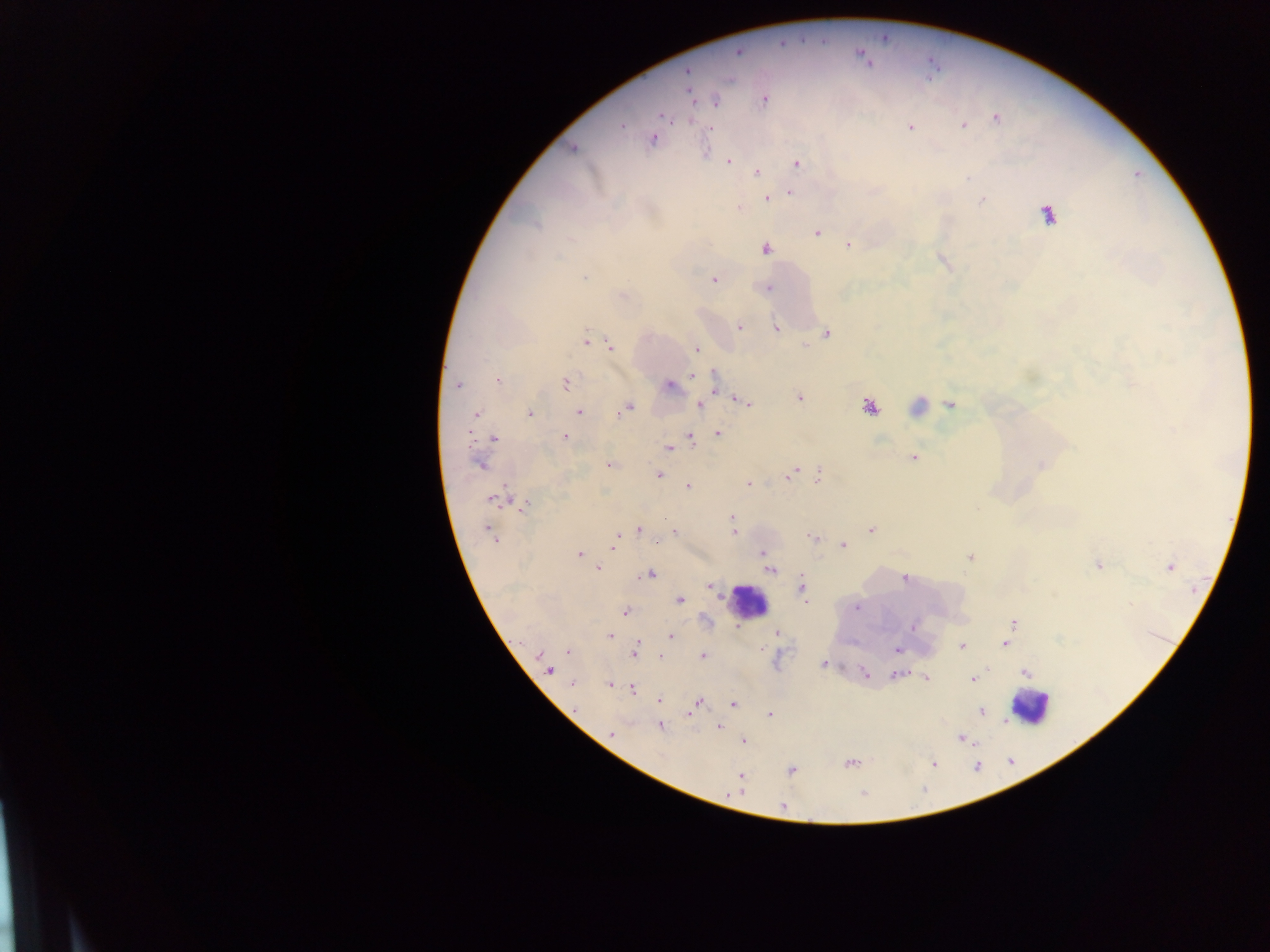

Approximate centers as x y in pixels.
Summary:
  - Leukocyte locations: 747 601; 1030 707
  - Plasmodium parasite locations: 738 52; 687 72; 691 95; 764 100; 716 101; 662 115; 996 118; 963 125; 621 126; 910 127; 710 129; 653 138; 574 148; 729 161; 797 164; 757 173; 790 193; 767 199; 983 200; 738 208; 1048 214; 817 233; 848 245; 766 249; 584 278; 713 279; 767 288; 739 327; 776 328; 827 334; 587 340; 611 347; 697 349; 692 375; 714 376; 498 380; 565 383; 459 385; 670 386; 799 397; 745 403; 700 405; 950 405; 870 406; 627 409; 578 412; 530 413; 476 414; 717 434; 690 436; 564 437; 494 438; 669 448; 914 457; 479 463; 609 465; 1042 465; 794 471; 659 475; 789 475; 818 475; 748 484; 688 486; 492 499; 525 505; 731 517; 665 518; 638 529; 871 529; 674 532; 733 533; 490 534; 813 538; 614 543; 657 543; 844 546; 763 553; 579 554; 969 557; 1098 565; 1169 567; 598 568; 771 571; 650 574; 904 579; 710 586; 801 589; 679 600; 857 607; 625 612; 1013 622; 912 626; 776 633; 610 636; 671 636; 1005 643; 637 645; 961 646; 897 649; 568 652; 635 653; 540 655; 703 656; 661 657; 823 664; 549 670; 864 673; 1025 673; 896 674; 926 679; 972 679; 573 684; 609 684; 633 690; 659 699; 696 703; 734 703; 575 709; 691 712; 981 712; 770 715; 660 726; 719 727; 611 733; 961 739; 744 741; 851 763; 934 763; 792 771; 740 776; 783 806
  - Field of view: single
  - Preparation: thick blood smear
  - Capture: mobile-phone photograph through a microscope
  - Image size: 1270×952 pixels
  - Country: Ghana